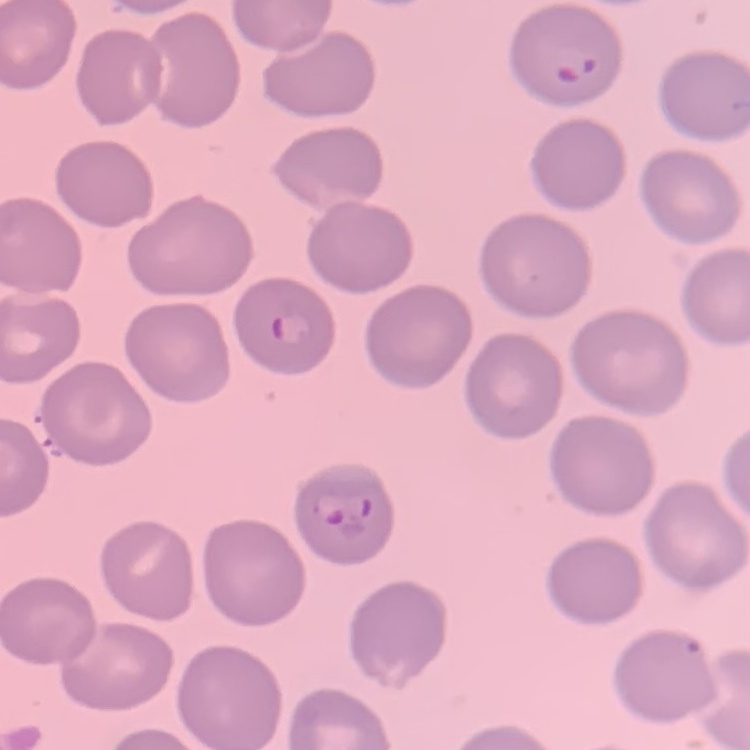

erythrocyte morphology = no rouleaux formation
image type = one tile cut from a larger photomicrograph
stain = Field's or Giemsa
preparation = thin blood film